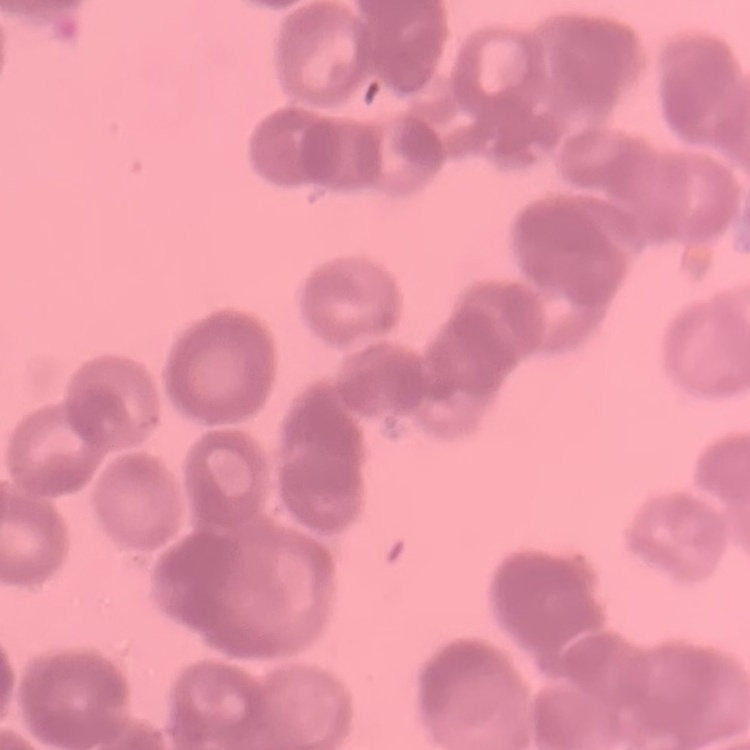
The erythrocytes exhibit rouleaux formation. One tile cut from a larger photomicrograph. Thin blood film. Field's or Giemsa stain.